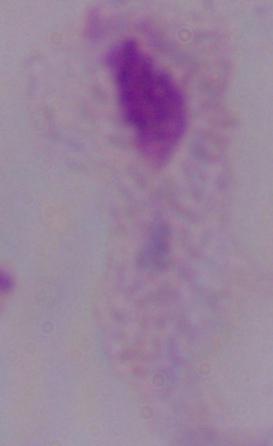

{
  "modality": "photomicrograph",
  "identification": "trichomonad",
  "magnification": "1000x"
}